Give the position of every malaria parasite.
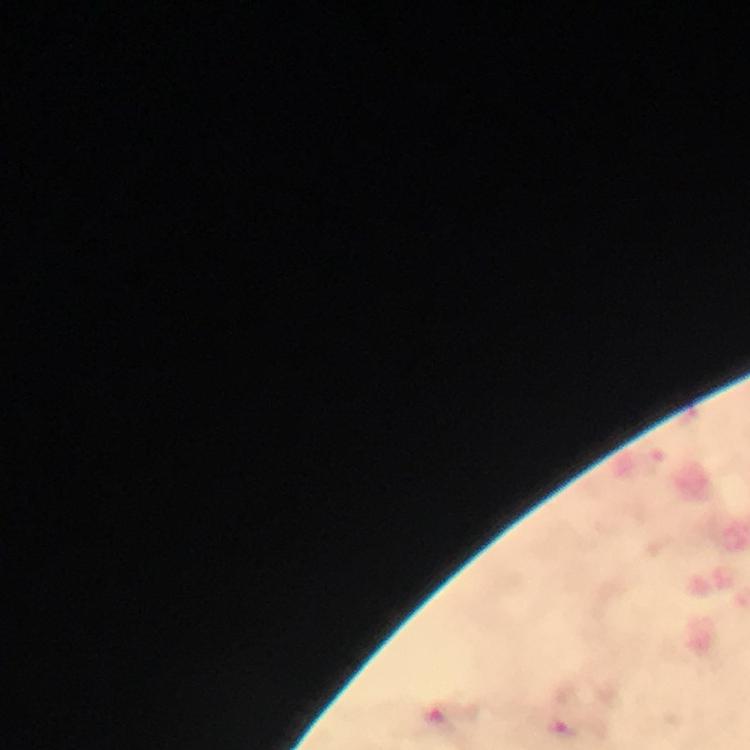

Approximate object centers, in pixels from the top-left corner.
Malaria parasites: (x=561, y=728).

capture = smartphone camera through the microscope
image size = 750×750 pixels
magnification = 100x
stain = Giemsa
immersion oil = used
preparation = thick blood smear
cropped from = a single field of view
context = from a malaria diagnostic workup